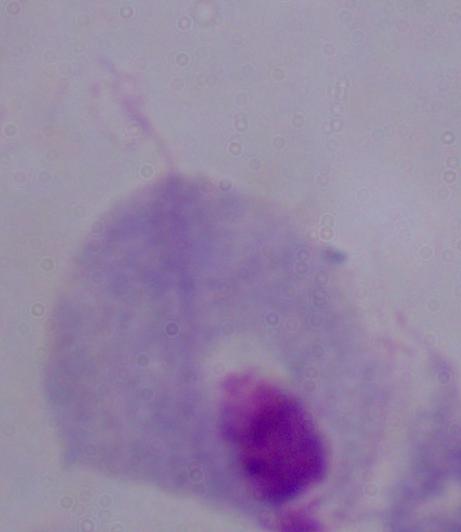

Summary:
  - Modality: photomicrograph
  - Identification: trichomonad
  - Magnification: 1000x